Classify this cell by malaria status.
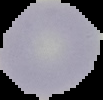

Uninfected.

Summary:
  - Preparation: thin blood film
  - Image type: segmented cell region on a black background
  - Image size: 103×100 pixels